State the blood parasite species.
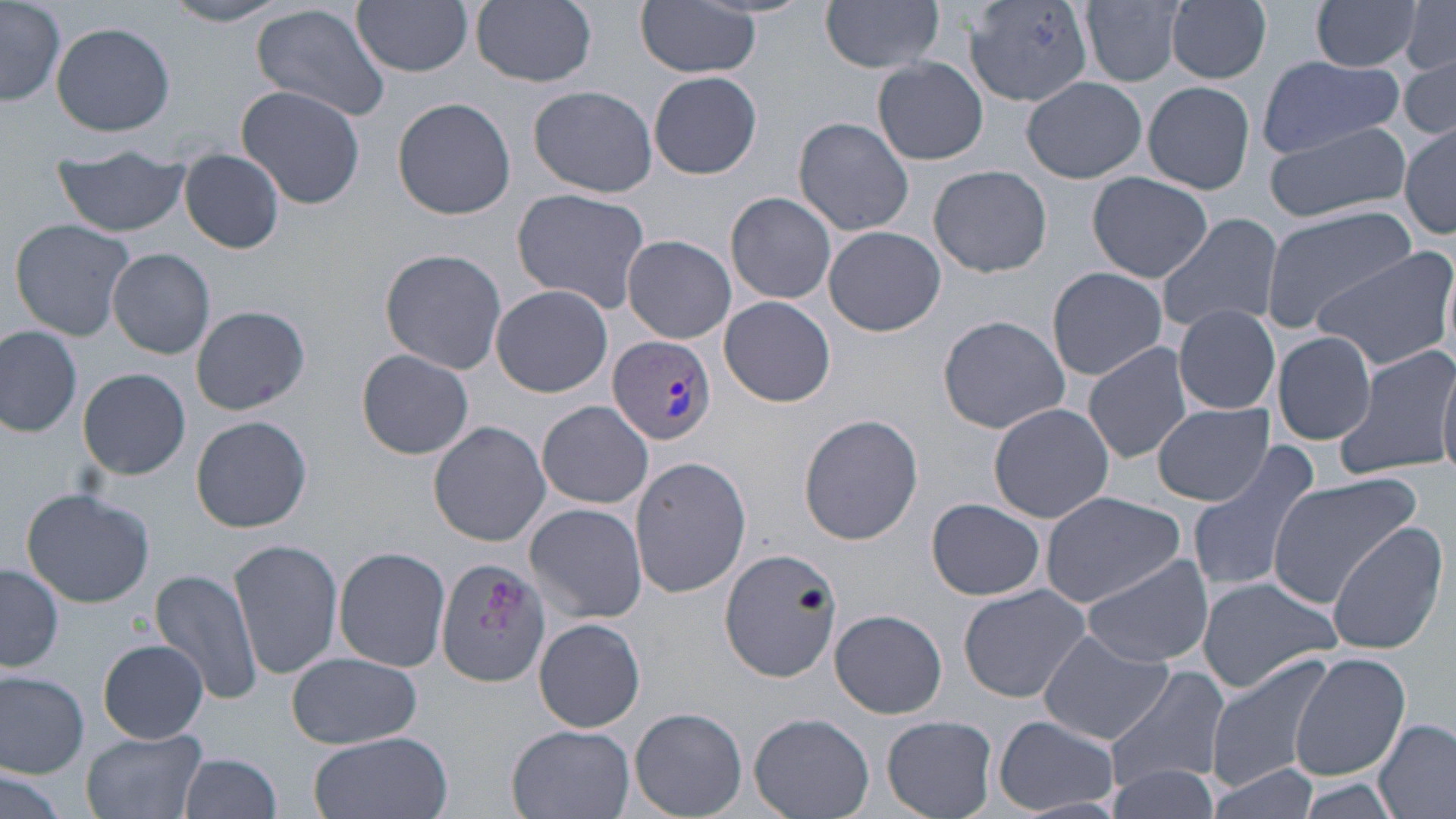

Plasmodium vivax.

Approximate bounding boxes as (x1,y1)-(x2,y2) corner pairs in pixels. Uninfected red blood cell locations: (1,0)-(64,106), (353,0)-(475,76), (471,0)-(596,88), (965,0)-(1097,106), (1080,0)-(1189,86), (1313,0)-(1422,73), (165,1)-(289,26), (637,1)-(762,78), (820,1)-(947,73), (1167,1)-(1272,83), (1399,2)-(1456,76), (250,3)-(392,122), (50,22)-(175,136), (1400,54)-(1456,141), (1256,55)-(1406,159), (873,57)-(987,164), (648,71)-(763,180), (1023,75)-(1146,184), (1143,81)-(1254,195), (528,84)-(658,198), (235,85)-(367,209), (392,96)-(515,220), (793,117)-(915,237), (1261,120)-(1411,223), (1401,124)-(1455,239), (180,149)-(286,253), (53,150)-(190,237), (928,165)-(1052,277), (1087,173)-(1211,282), (512,188)-(654,314), (726,192)-(837,306), (1258,203)-(1420,332), (1156,213)-(1284,337), (9,217)-(136,341), (823,226)-(947,336), (621,235)-(736,343), (1312,245)-(1456,370), (108,248)-(215,359), (379,249)-(508,374), (1046,266)-(1169,381), (490,285)-(614,398), (719,296)-(837,407), (191,304)-(310,416), (1173,305)-(1280,414), (938,315)-(1070,432), (0,325)-(81,439), (1272,331)-(1377,444), (1082,342)-(1194,464), (1335,343)-(1452,480), (355,350)-(475,459), (1437,359)-(1456,479), (78,367)-(191,480), (537,402)-(655,510), (986,402)-(1116,523), (1151,403)-(1275,505), (191,414)-(311,532), (798,414)-(924,545), (428,421)-(551,546), (1185,441)-(1323,595), (628,456)-(749,598), (1264,472)-(1424,610), (20,487)-(155,608), (1039,490)-(1188,606), (926,499)-(1045,602), (525,502)-(650,623), (1326,524)-(1449,653), (229,538)-(342,680), (334,546)-(450,674), (720,547)-(841,681), (1080,554)-(1214,668), (435,555)-(552,686), (1,562)-(64,672), (152,566)-(263,702), (1194,575)-(1343,695), (957,584)-(1093,703), (829,609)-(947,719), (533,618)-(647,732), (1037,628)-(1171,745), (98,637)-(208,743), (1289,652)-(1410,781), (285,653)-(423,750), (1205,653)-(1338,790), (1105,666)-(1232,791), (0,669)-(90,776), (630,707)-(746,818), (750,711)-(874,817), (992,714)-(1119,815), (882,715)-(997,818), (1375,718)-(1455,819), (506,725)-(635,819), (79,730)-(211,819), (309,730)-(451,819), (178,753)-(282,819), (1205,764)-(1316,818), (1105,765)-(1218,819), (0,768)-(69,818), (1298,781)-(1403,819). Plasmodium vivax-infected red blood cell locations: (609,335)-(716,446). Single field of view. Image is 1456×819 pixels. 1000x magnification. May-Grünwald-Giemsa-stained preparation. Thin blood film. Optical microscopy.